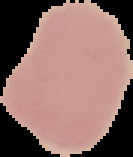
Image is 133×157 pixels. Cell region segmented out of the field of view; the surrounding area is masked to black. From a thin blood smear. Result: negative for malaria parasites.